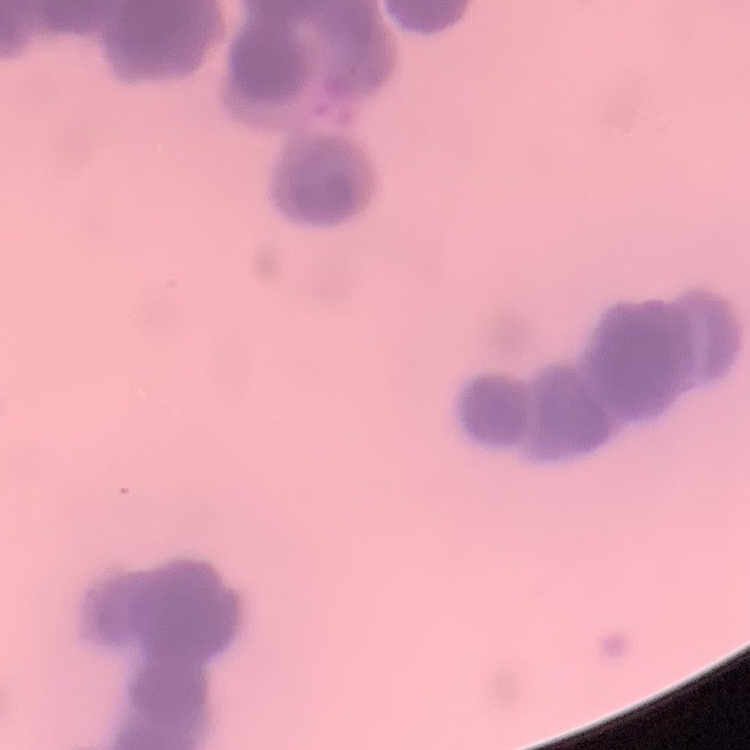

erythrocyte morphology = rouleaux formation
preparation = thin blood smear
stain = Field's or Giemsa
image type = square crop of a larger photomicrograph